State which parasite is depicted.
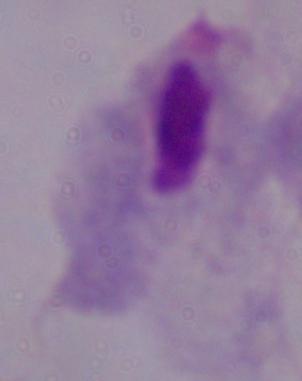

This is a trichomonad.

modality: photomicrograph
magnification: 1000x